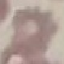

Summary:
  - Result: no malaria parasites detected
  - Image type: cell patch, automatically extracted from a larger field of view and resized to 64 × 64 pixels
  - Capture: smartphone camera at the microscope eyepiece
  - Preparation: thin smear
  - Stain: Giemsa